Identify the cell.
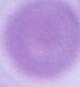

An erythrocyte.

Summary:
  - Magnification: 1000x
  - Modality: photomicrograph